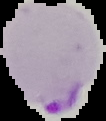

image size = 106×121 pixels
result = malaria parasites identified
image type = cell region segmented out of the field of view; surrounding area masked to black
preparation = thin blood smear